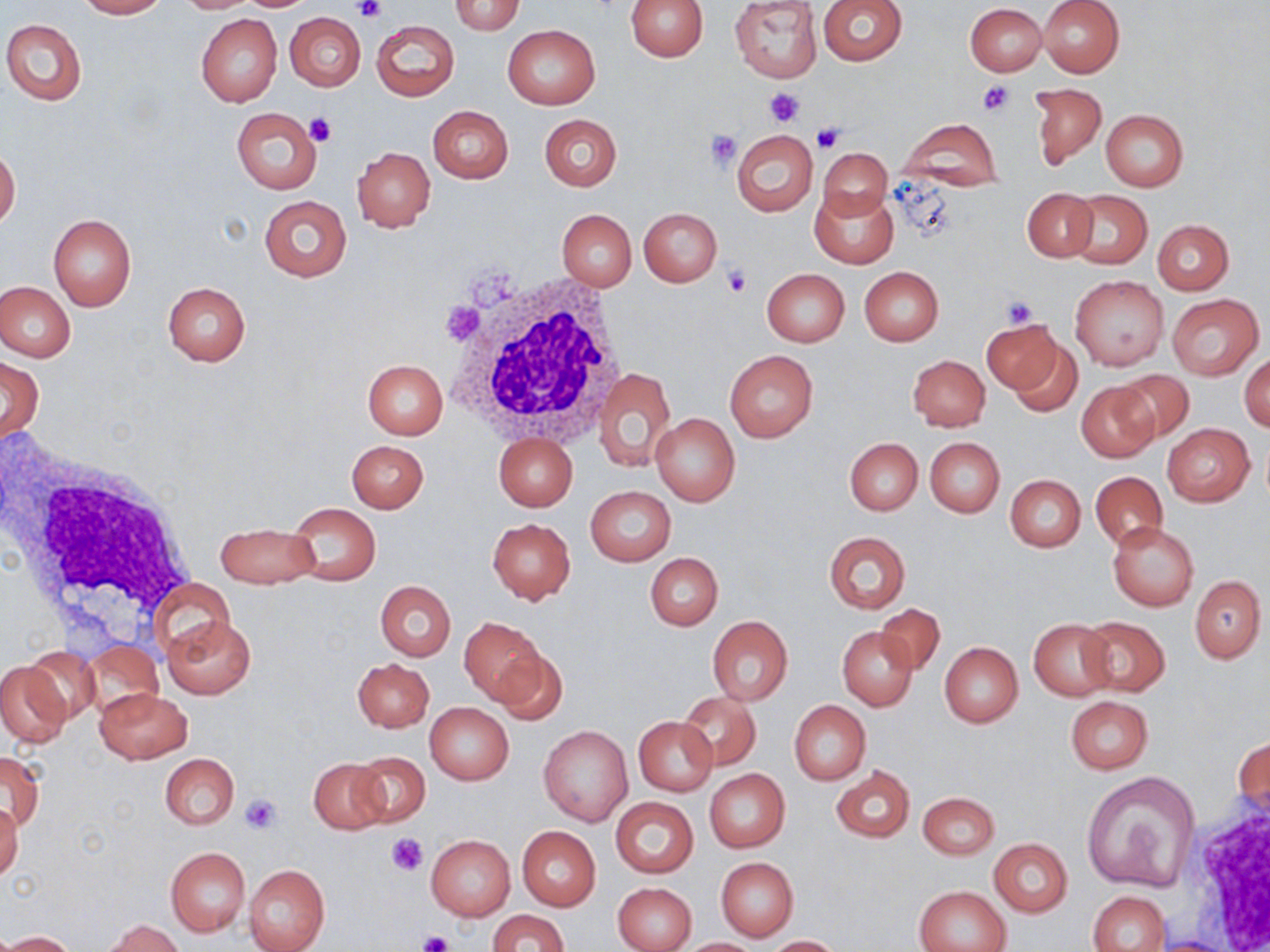
{
  "slide_level_diagnosis": "no evidence of blood parasites",
  "magnification": "1000x",
  "uninfected_red_blood_cell_locations": "approximate bounding boxes as (x1, y1, x2, y2) in pixels: (75, 0, 165, 18), (174, 0, 261, 13), (241, 0, 312, 10), (626, 0, 709, 62), (729, 0, 822, 83), (817, 0, 907, 65), (1039, 0, 1124, 78), (449, 1, 525, 35), (964, 3, 1047, 76), (285, 12, 366, 91), (196, 13, 282, 107), (2, 19, 87, 105), (372, 20, 459, 101), (502, 25, 600, 108), (1029, 82, 1106, 169), (428, 105, 513, 184), (231, 107, 321, 193), (1101, 110, 1188, 190), (539, 114, 621, 191), (899, 118, 1005, 190), (731, 130, 818, 216), (818, 145, 894, 221), (0, 146, 21, 230), (352, 147, 435, 231), (1021, 187, 1097, 262), (810, 188, 898, 267), (1066, 191, 1152, 270), (259, 195, 350, 282), (638, 208, 721, 287), (557, 209, 637, 290), (48, 214, 137, 311), (1152, 219, 1234, 294), (859, 266, 944, 346), (761, 268, 849, 346), (1071, 275, 1167, 371), (0, 281, 75, 361), (162, 281, 251, 366), (1166, 293, 1264, 381), (984, 317, 1068, 402), (1003, 334, 1088, 420), (724, 351, 818, 443), (1240, 351, 1270, 432), (0, 355, 43, 443), (909, 355, 990, 431), (362, 360, 448, 439), (595, 367, 676, 473), (1110, 369, 1195, 447), (1076, 382, 1160, 462), (652, 413, 740, 506), (1162, 424, 1254, 506), (494, 433, 577, 510), (925, 437, 1004, 516), (845, 438, 922, 515), (347, 440, 428, 513), (1090, 471, 1168, 549), (1006, 475, 1085, 551), (586, 487, 676, 566), (286, 502, 381, 585), (487, 517, 576, 604), (217, 521, 320, 590), (1108, 522, 1198, 611), (823, 532, 910, 612), (645, 553, 723, 630), (1189, 575, 1266, 663), (151, 580, 235, 661), (376, 580, 455, 661), (875, 603, 945, 676), (1077, 615, 1170, 696), (162, 616, 255, 699), (706, 616, 793, 706), (458, 617, 548, 706), (1028, 619, 1116, 701), (838, 626, 918, 710), (83, 641, 161, 717), (489, 643, 568, 723), (940, 643, 1022, 727), (26, 646, 101, 725), (352, 657, 433, 732), (0, 659, 71, 748), (96, 687, 191, 764), (678, 691, 761, 770), (1065, 696, 1153, 774), (789, 700, 871, 785), (425, 702, 513, 785), (633, 717, 717, 795), (539, 725, 632, 826), (1233, 730, 1270, 820), (2, 750, 43, 833), (350, 750, 430, 827), (160, 753, 239, 829), (310, 757, 389, 833), (831, 765, 915, 842), (704, 770, 790, 852), (1081, 770, 1202, 893), (918, 791, 998, 859), (611, 797, 698, 878), (0, 803, 23, 881), (517, 826, 601, 911), (426, 835, 514, 920), (988, 838, 1073, 916), (165, 847, 249, 936), (716, 858, 798, 940), (243, 864, 330, 952), (614, 882, 696, 952), (914, 886, 1011, 952), (1089, 890, 1170, 951), (488, 909, 568, 952), (103, 919, 182, 952), (3, 930, 75, 951), (768, 935, 842, 951), (679, 937, 763, 951)",
  "preparation": "thin blood film",
  "image_size": "1270×952 pixels",
  "stain": "May-Grünwald-Giemsa",
  "platelet_locations": "approximate bounding boxes as (x1, y1, x2, y2) in pixels: (353, 0, 386, 23), (977, 79, 1014, 116), (766, 88, 806, 125), (304, 112, 337, 147), (811, 125, 843, 153), (706, 129, 742, 169), (723, 265, 751, 297), (1002, 297, 1039, 328), (239, 794, 283, 833), (389, 833, 428, 875), (417, 930, 454, 952)",
  "white_blood_cell_locations": "approximate bounding boxes as (x1, y1, x2, y2) in pixels: (441, 267, 630, 446), (3, 443, 199, 632), (1180, 783, 1270, 952)",
  "modality": "optical microscopy",
  "field_of_view": "single"
}